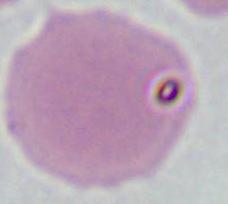

modality = photomicrograph
identification = red blood cell
magnification = 1000x